Comment on the morphology of the erythrocytes.
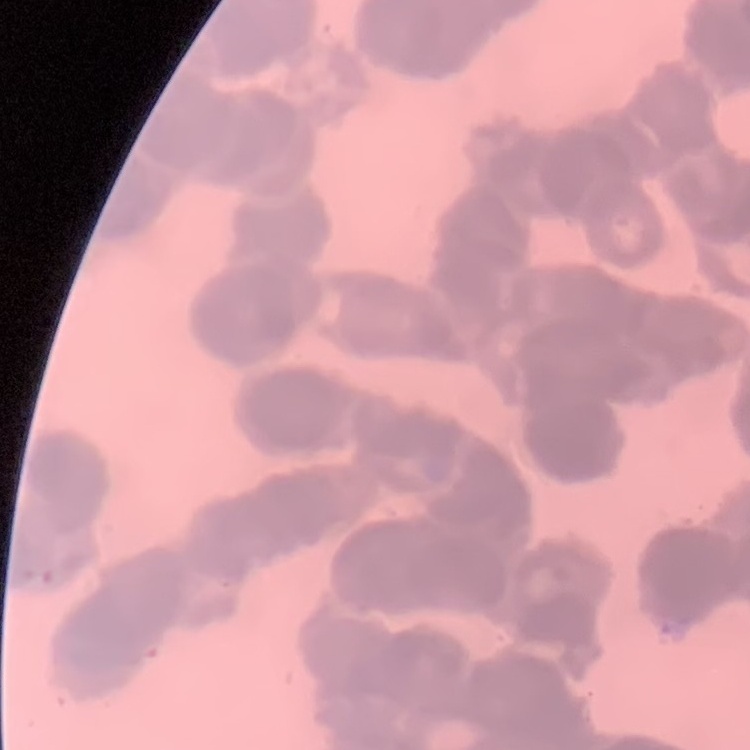

Rouleaux formation.

Summary:
  - Stain: Field's or Giemsa
  - Preparation: thin peripheral smear
  - Image type: square crop of a larger photomicrograph